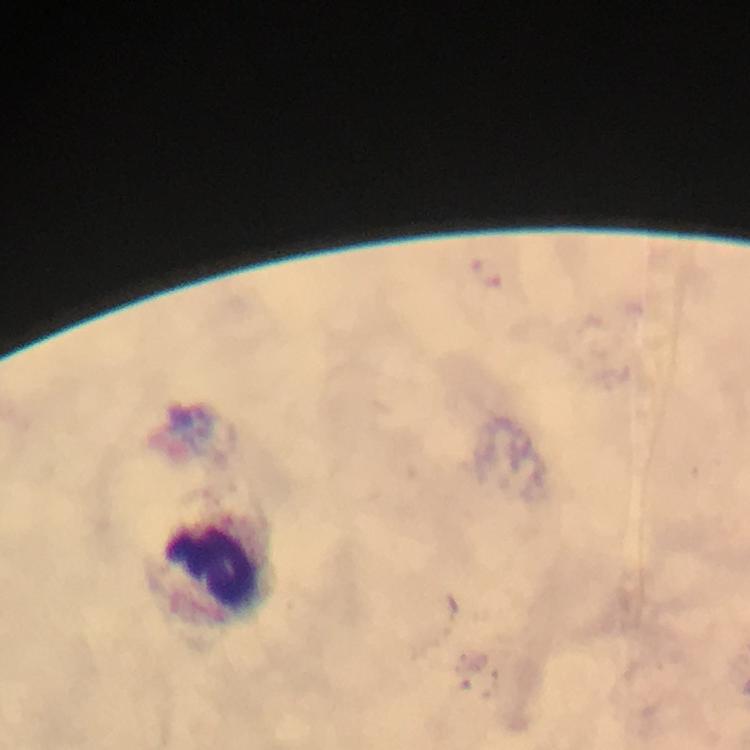
Approximate centers as (x, y) in pixels.
Summary:
  - Leukocyte locations: (218, 570)
  - Magnification: 100x
  - Preparation: thick blood film
  - Capture: smartphone photograph through a microscope
  - Image size: 750×750 pixels
  - Cropped from: one field of view
  - Stain: Giemsa
  - Immersion oil: applied
  - Malaria parasites: none detected
  - Context: from a malaria diagnostic workup